Look for Plasmodium parasites.
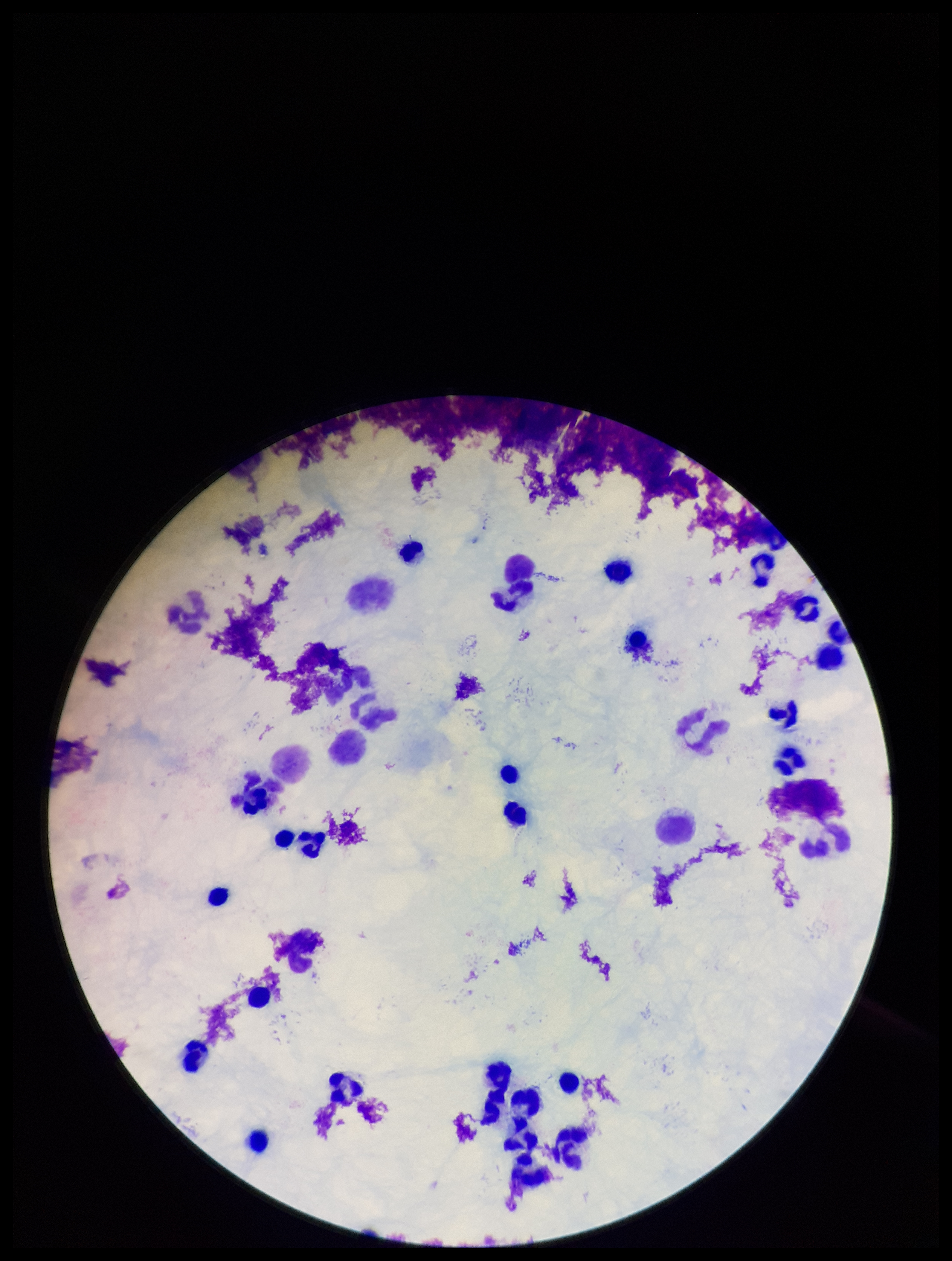
None detected.

Summary:
  - Patient malaria status: negative
  - Image size: 952×1261 pixels
  - Stain: Giemsa
  - Preparation: thick blood smear
  - Capture: smartphone photograph through the microscope eyepiece
  - Field of view: single
  - Parasite count: 0
  - Leukocyte count: 28